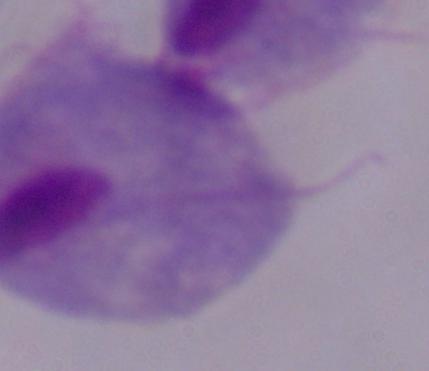
Summary:
  - Modality: micrograph
  - Identification: trichomonad
  - Magnification: 1000x